Report the malaria status.
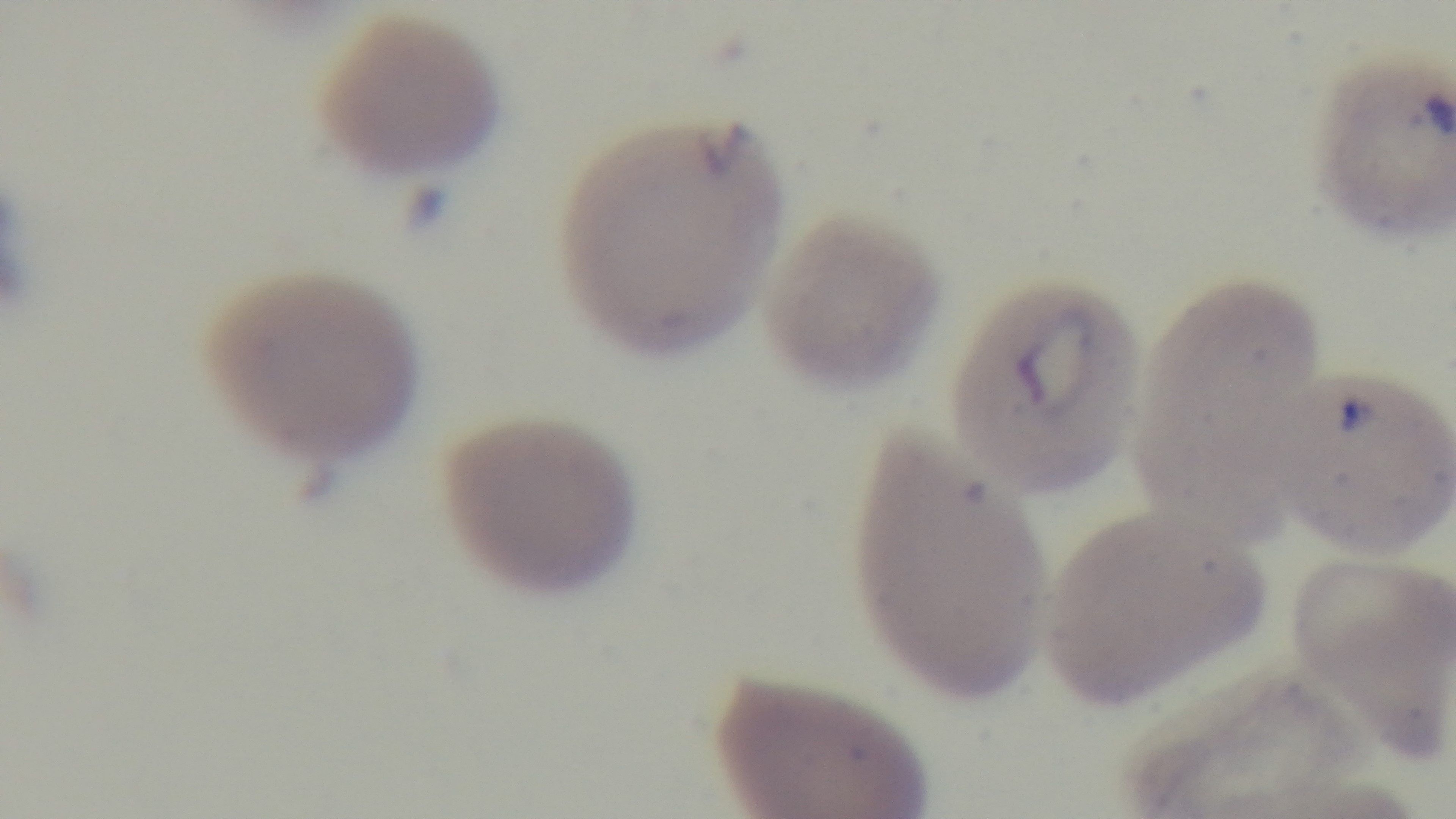
It is infected.

Oil-immersion objective, 100x. Light microscopy. One field from the slide. Giemsa-stained. Captured with a mounted 4K digital camera. Preparation: thin.